Report the malaria status of this cell.
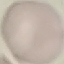

It is uninfected.

Summary:
  - Stain: Giemsa
  - Preparation: thin blood smear
  - Capture: smartphone camera at the microscope eyepiece
  - Image type: automatically extracted cell patch, resized to 64 × 64 pixels